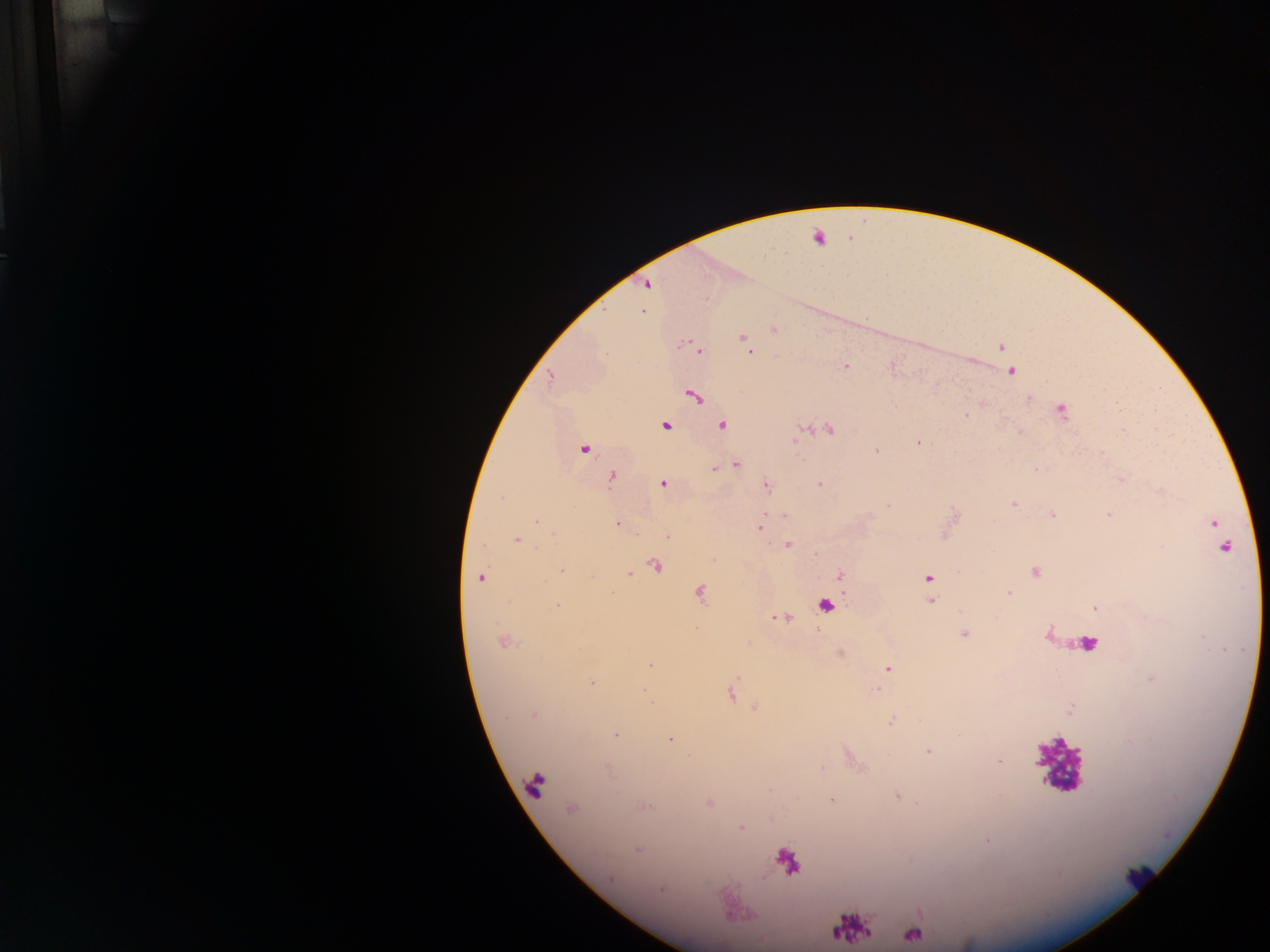

Approximate centers as [x, y] in pixels.
Summary:
  - Leukocyte locations: [817, 237], [827, 605], [1082, 642], [1058, 764], [535, 785]
  - Object labeled both malaria parasite and leukocyte by the source: [786, 860]
  - Malaria parasite locations: [646, 284], [643, 311], [774, 329], [743, 338], [1001, 347], [700, 351], [749, 351], [846, 365], [1012, 372], [550, 378], [694, 396], [1061, 410], [966, 416], [722, 425], [665, 426], [829, 430], [919, 442], [583, 449], [876, 450], [735, 464], [715, 469], [1035, 469], [611, 477], [663, 483], [819, 484], [766, 486], [501, 497], [1013, 504], [1109, 515], [784, 516], [535, 522], [1214, 523], [617, 524], [760, 528], [668, 537], [516, 540], [789, 545], [1224, 547], [714, 560], [655, 566], [562, 571], [1036, 571], [629, 574], [839, 575], [480, 578], [928, 578], [1008, 592], [699, 593], [931, 601], [558, 605], [1095, 608], [964, 634], [504, 643], [650, 665], [888, 669], [591, 682], [876, 690], [731, 694], [533, 715], [891, 721], [616, 735], [669, 739], [928, 751], [897, 795], [832, 799], [710, 802], [646, 806], [571, 810], [741, 828], [637, 849], [611, 879], [661, 890], [913, 935]
  - Country: Ghana
  - Capture: mobile-phone photograph through a microscope
  - Preparation: thick blood smear
  - Field of view: single
  - Image size: 1270×952 pixels